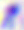
Toxoplasma gondii is seen. Micrograph. 400x magnification.